Assess the morphology of the erythrocytes.
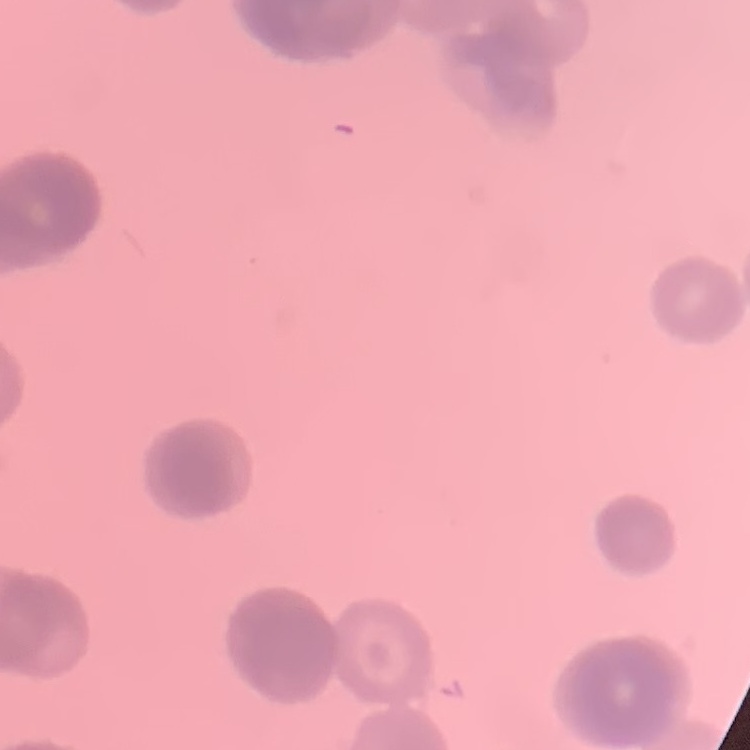
They show rouleaux formation.

stain: Field's or Giemsa
preparation: thin peripheral smear
image_type: square crop of a larger photomicrograph